Name the parasite shown.
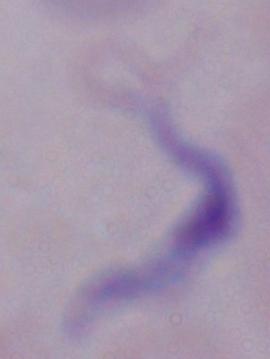
This is a trypanosome.

Summary:
  - Modality: micrograph
  - Magnification: 1000x